State which parasite is depicted.
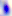

Toxoplasma gondii.

Summary:
  - Modality: photomicrograph
  - Magnification: 400x